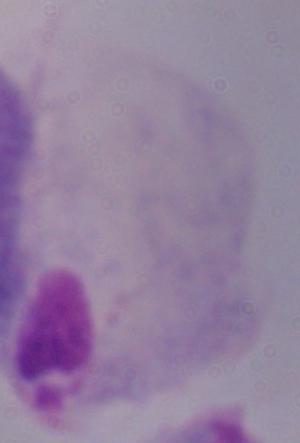

magnification: 1000x
modality: micrograph
identification: trichomonad